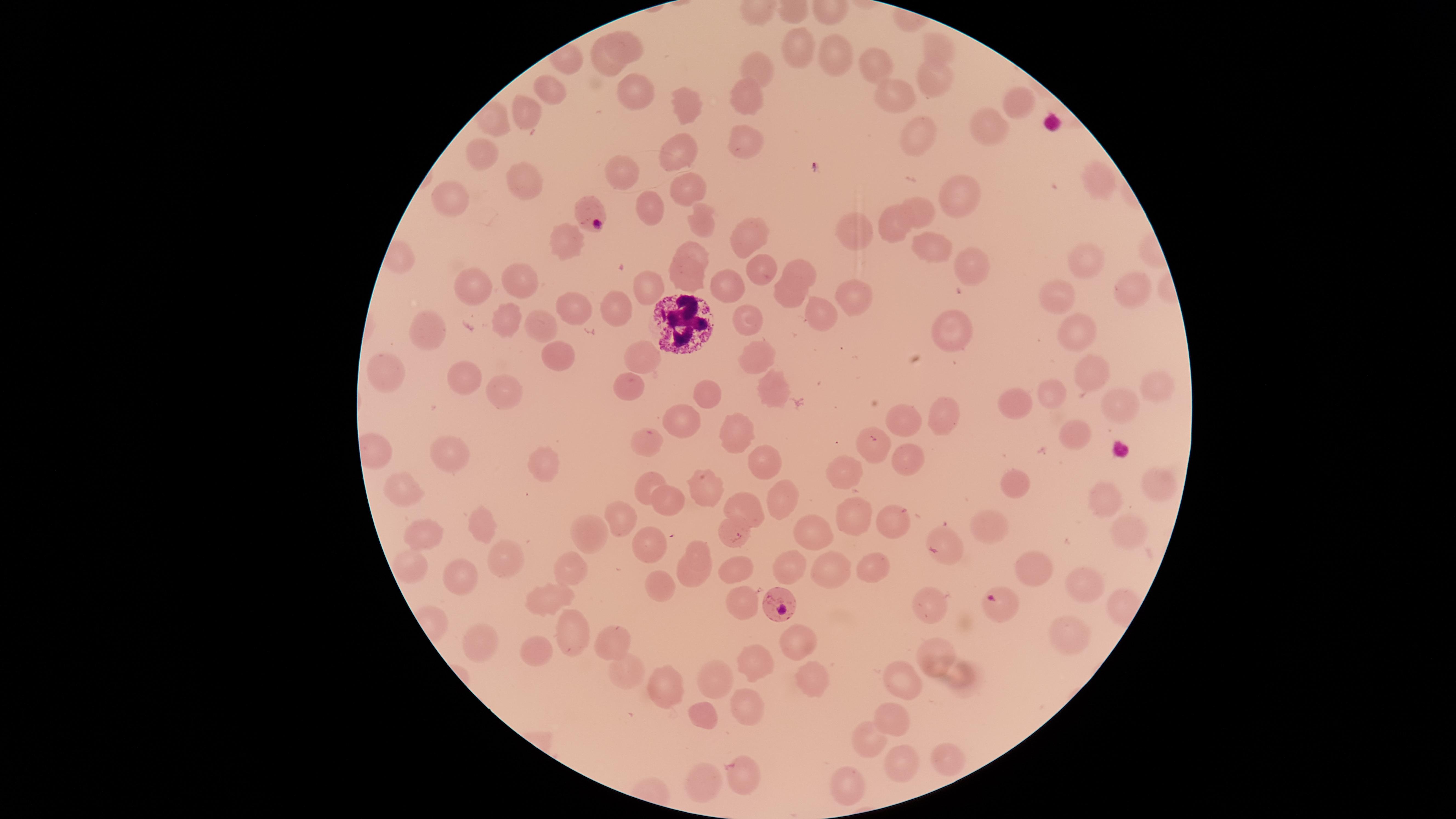
Approximate marker points as (x, y) in pixels.
Summary:
  - Uninfected RBCs: (621, 43), (934, 46), (801, 49), (836, 58), (599, 63), (873, 65), (763, 66), (933, 80), (553, 91), (750, 91), (894, 91), (634, 93), (1014, 102), (681, 107), (523, 118), (993, 131), (916, 135), (749, 138), (483, 150), (678, 155), (618, 170), (1098, 179), (525, 183), (684, 189), (965, 194), (649, 204), (449, 208), (923, 211), (698, 213), (852, 227), (743, 233), (891, 233), (693, 248), (937, 253), (1087, 259), (971, 265), (802, 268), (762, 269), (523, 275), (473, 279), (682, 279), (1127, 284), (647, 287), (726, 287), (1055, 294), (860, 296), (785, 300), (572, 303), (614, 307), (822, 314), (506, 318), (745, 318), (542, 321), (428, 325), (1071, 326), (954, 327), (558, 354), (641, 354), (759, 360), (1092, 365), (387, 372), (459, 378), (1154, 380), (626, 388), (706, 389), (775, 391), (499, 392), (1052, 395), (1115, 400), (1018, 401), (945, 411), (679, 419), (913, 419), (737, 429), (1072, 431), (652, 438), (868, 445), (905, 454), (450, 459), (761, 459), (538, 464), (841, 470), (650, 483), (1016, 483), (1158, 485), (407, 488), (709, 488), (1106, 498), (668, 504), (741, 508), (782, 508), (850, 516), (888, 517), (624, 521), (995, 524), (477, 527), (811, 527), (1127, 527), (418, 531), (588, 532), (732, 532), (651, 544), (699, 550), (500, 558), (409, 563), (792, 563), (870, 566), (834, 567), (572, 569), (738, 571), (1034, 572), (458, 576), (689, 577), (1080, 587), (659, 589), (552, 596), (931, 597), (740, 606), (572, 630), (1063, 634), (798, 635), (479, 638), (613, 642), (938, 645), (536, 646), (749, 663), (625, 667), (718, 674), (810, 677), (899, 679), (959, 686), (660, 688), (740, 704), (705, 712), (894, 721), (866, 737), (947, 752), (896, 758), (742, 776), (696, 782), (841, 782)
  - Parasitized RBCs: (589, 212), (1000, 602), (780, 604)
  - WBCs: (680, 319)
  - Preparation: thin blood smear
  - Stain: Giemsa
  - Presence: malaria parasites seen
  - Visible region: circular
  - Species: Plasmodium falciparum
  - Field of view: single
  - Image size: 1456×819 pixels
  - Capture: smartphone photograph through the microscope eyepiece